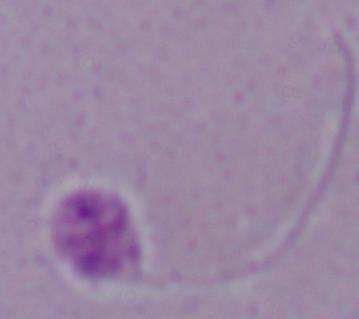
Photomicrograph. 1000x magnification. A Leishmania parasite is shown.